Report the malaria status of this cell.
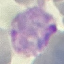
Parasitized.

Thin blood smear. Photographed with a smartphone camera at the microscope eyepiece. Cell patch, automatically extracted from a larger field of view and resized to 64 × 64 pixels. Giemsa stain.